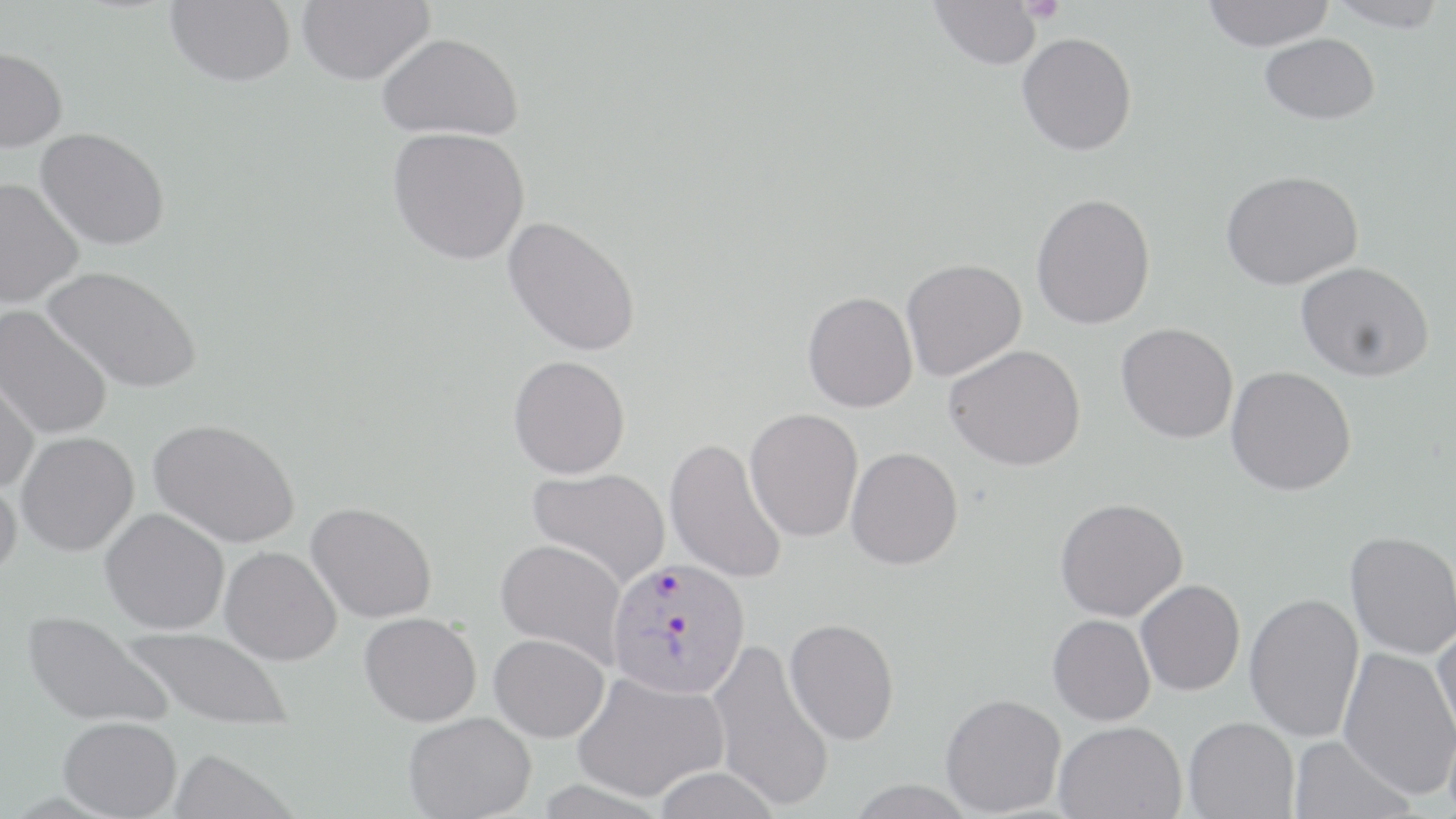
Summary:
  - Coordinate format: approximate bounding boxes as named x1/y1/x2/y2 corners in pixels
  - Platelet locations: (x1=1019, y1=0, x2=1065, y2=25)
  - Uninfected red blood cell locations: (x1=297, y1=0, x2=433, y2=85), (x1=929, y1=0, x2=1043, y2=69), (x1=1202, y1=0, x2=1335, y2=51), (x1=1324, y1=0, x2=1450, y2=32), (x1=165, y1=1, x2=296, y2=86), (x1=378, y1=32, x2=523, y2=140), (x1=1017, y1=32, x2=1137, y2=155), (x1=1259, y1=33, x2=1380, y2=124), (x1=0, y1=46, x2=67, y2=152), (x1=36, y1=126, x2=171, y2=251), (x1=389, y1=127, x2=531, y2=265), (x1=1220, y1=170, x2=1363, y2=290), (x1=0, y1=176, x2=84, y2=308), (x1=1031, y1=192, x2=1156, y2=329), (x1=503, y1=215, x2=642, y2=357), (x1=901, y1=258, x2=1026, y2=381), (x1=1296, y1=261, x2=1434, y2=381), (x1=43, y1=265, x2=203, y2=394), (x1=803, y1=291, x2=918, y2=412), (x1=0, y1=304, x2=114, y2=441), (x1=1116, y1=322, x2=1238, y2=443), (x1=944, y1=343, x2=1085, y2=470), (x1=508, y1=355, x2=631, y2=478), (x1=0, y1=363, x2=40, y2=493), (x1=1226, y1=365, x2=1356, y2=495), (x1=745, y1=408, x2=864, y2=542), (x1=149, y1=417, x2=301, y2=549), (x1=16, y1=430, x2=140, y2=556), (x1=665, y1=437, x2=787, y2=584), (x1=846, y1=446, x2=963, y2=570), (x1=527, y1=467, x2=670, y2=588), (x1=0, y1=472, x2=23, y2=581), (x1=1055, y1=498, x2=1188, y2=621), (x1=306, y1=502, x2=437, y2=623), (x1=100, y1=508, x2=230, y2=634), (x1=1345, y1=530, x2=1455, y2=659), (x1=496, y1=539, x2=626, y2=664), (x1=220, y1=546, x2=342, y2=665), (x1=1136, y1=579, x2=1245, y2=695), (x1=1244, y1=592, x2=1364, y2=742), (x1=23, y1=611, x2=171, y2=729), (x1=360, y1=612, x2=482, y2=726), (x1=1048, y1=614, x2=1156, y2=726), (x1=784, y1=618, x2=900, y2=745), (x1=1432, y1=624, x2=1456, y2=750), (x1=122, y1=625, x2=295, y2=732), (x1=489, y1=633, x2=609, y2=742), (x1=708, y1=638, x2=835, y2=812), (x1=1338, y1=646, x2=1456, y2=799), (x1=572, y1=671, x2=729, y2=802), (x1=940, y1=693, x2=1066, y2=816), (x1=403, y1=712, x2=536, y2=819), (x1=58, y1=716, x2=182, y2=818), (x1=1183, y1=716, x2=1298, y2=818), (x1=1055, y1=720, x2=1186, y2=818), (x1=1288, y1=734, x2=1416, y2=819), (x1=169, y1=748, x2=296, y2=819), (x1=651, y1=767, x2=783, y2=819), (x1=844, y1=780, x2=978, y2=819)
  - Plasmodium vivax-infected red blood cell locations: (x1=607, y1=558, x2=750, y2=698)
  - Slide-level diagnosis: Plasmodium vivax
  - Modality: optical microscopy
  - Image size: 1456×819 pixels
  - Preparation: thin blood smear
  - Field of view: one of a larger specimen
  - Stain: May-Grünwald-Giemsa
  - Magnification: 1000x